Assess the morphology of the erythrocytes.
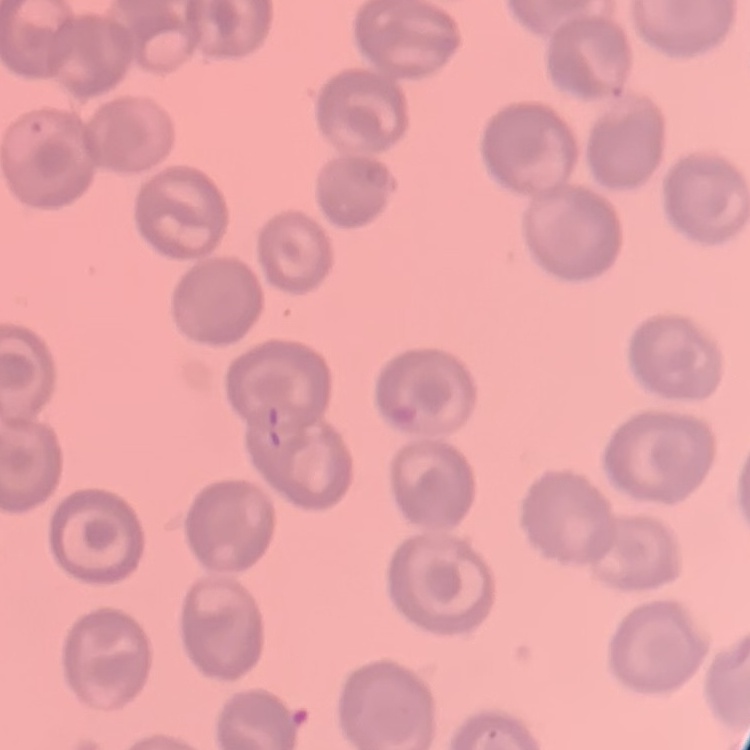
No rouleaux formation.

Summary:
  - Stain: Field's or Giemsa
  - Preparation: thin blood smear
  - Image type: one tile cut from a larger photomicrograph